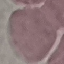

Summary:
  - Malaria status: uninfected
  - Image type: automatically extracted cell patch, resized to 64 × 64 pixels
  - Preparation: thin blood film
  - Stain: Giemsa
  - Capture: smartphone camera at the microscope eyepiece